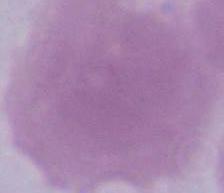

Micrograph. An erythrocyte is seen. 1000x magnification.